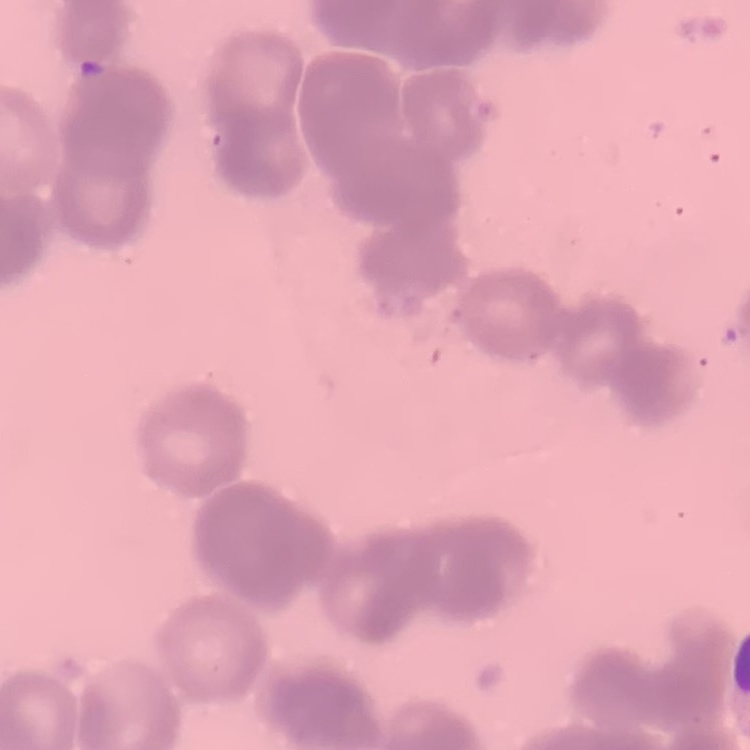

erythrocyte morphology = rouleaux formation
preparation = thin blood smear
image type = one tile cut from a larger photomicrograph
stain = Field's or Giemsa